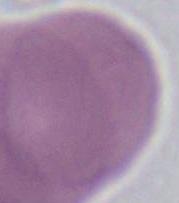
Summary:
  - Magnification: 1000x
  - Identification: erythrocyte
  - Modality: photomicrograph